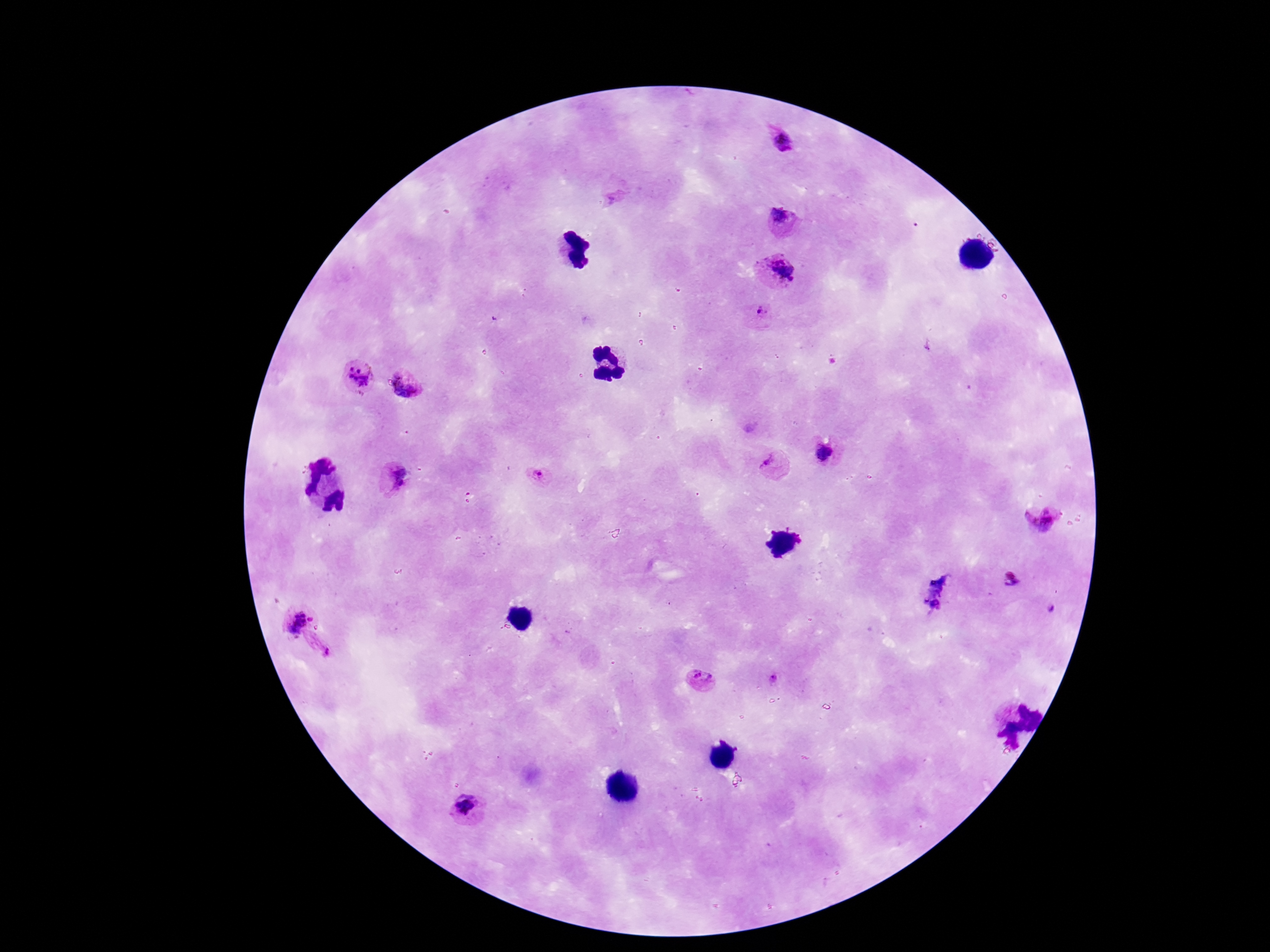 Approximate centers as [x, y] in pixels. Plasmodium parasite locations: [781, 142], [783, 220], [779, 269], [759, 314], [360, 376], [404, 385], [825, 454], [773, 464], [540, 474], [395, 478], [1041, 518], [297, 623], [320, 645], [703, 680], [466, 807]. Thick peripheral-blood smear. Single field of view. Image is 1270×952 pixels. Smartphone photograph taken through the microscope eyepiece. 100x magnification. Giemsa stain. Patient malaria status: infected.